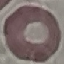
Malaria status: uninfected. Photographed with a smartphone camera at the microscope eyepiece. Giemsa-stained preparation. Thin blood smear. Automatically extracted cell patch, resized to 64 × 64 pixels.